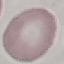

Summary:
  - Malaria status: uninfected
  - Capture: smartphone through the microscope eyepiece
  - Stain: Giemsa
  - Image type: automatically extracted cell patch, resized to 64 × 64 pixels
  - Preparation: thin blood film